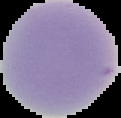

From a thin blood smear. Malaria status: uninfected. Cell region segmented out of the field of view; the surrounding area is masked to black. Image is 121×118 pixels.